Assess this cell for malaria.
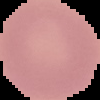
Uninfected.

preparation = thin blood film
image size = 100×100 pixels
image type = cell region segmented out of the field of view; surrounding area masked to black